Outline each blood parasite and name the species.
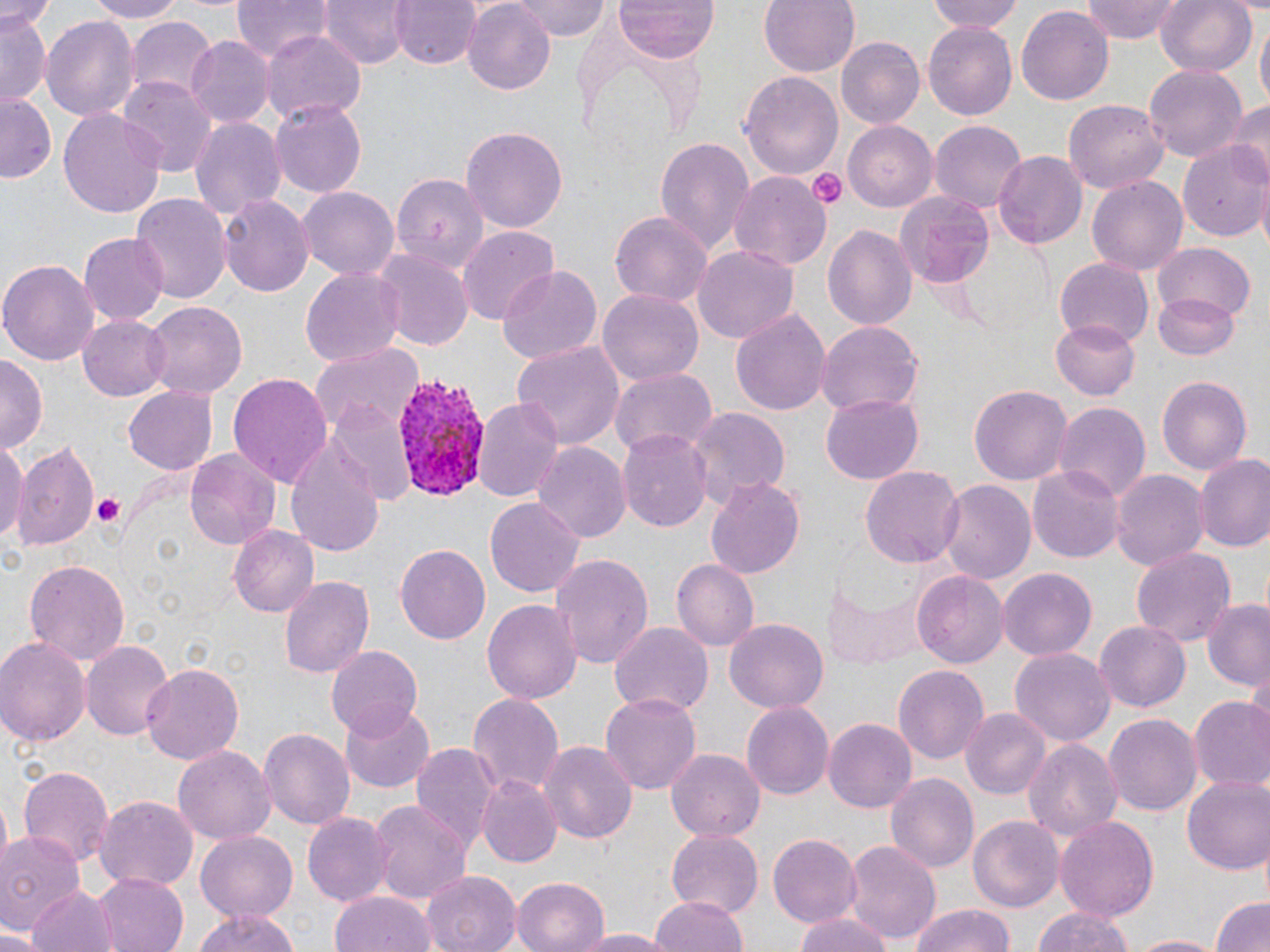

Approximate bounding boxes as named x1/y1/x2/y2 corners in pixels.
Plasmodium vivax-infected red blood cells: (x1=393, y1=371, x2=491, y2=504).
No Plasmodium falciparum, Plasmodium ovale, Plasmodium malariae, Babesia divergens, or Trypanosoma brucei observed.

slide-level diagnosis = Plasmodium vivax
magnification = 1000x
stain = May-Grünwald-Giemsa
platelet locations = approximate bounding boxes as named x1/y1/x2/y2 corners in pixels: (x1=808, y1=169, x2=847, y2=208), (x1=89, y1=493, x2=128, y2=530)
modality = optical microscopy
field of view = single
image size = 1270×952 pixels
preparation = thin blood smear
uninfected red blood cell locations = approximate bounding boxes as named x1/y1/x2/y2 corners in pixels: (x1=0, y1=0, x2=56, y2=28), (x1=81, y1=0, x2=192, y2=22), (x1=232, y1=0, x2=327, y2=62), (x1=318, y1=0, x2=411, y2=68), (x1=393, y1=0, x2=479, y2=69), (x1=511, y1=0, x2=609, y2=41), (x1=613, y1=0, x2=718, y2=62), (x1=757, y1=0, x2=859, y2=77), (x1=928, y1=0, x2=1023, y2=35), (x1=1080, y1=0, x2=1184, y2=42), (x1=1153, y1=0, x2=1256, y2=77), (x1=1015, y1=3, x2=1114, y2=104), (x1=462, y1=4, x2=557, y2=94), (x1=0, y1=8, x2=48, y2=108), (x1=41, y1=12, x2=139, y2=121), (x1=125, y1=17, x2=216, y2=102), (x1=1255, y1=19, x2=1269, y2=112), (x1=924, y1=20, x2=1019, y2=120), (x1=262, y1=30, x2=364, y2=124), (x1=186, y1=37, x2=274, y2=127), (x1=834, y1=37, x2=924, y2=130), (x1=1143, y1=65, x2=1248, y2=163), (x1=739, y1=68, x2=844, y2=180), (x1=118, y1=78, x2=216, y2=175), (x1=0, y1=95, x2=56, y2=183), (x1=1222, y1=95, x2=1270, y2=183), (x1=1062, y1=98, x2=1168, y2=195), (x1=271, y1=101, x2=370, y2=197), (x1=59, y1=108, x2=166, y2=218), (x1=190, y1=116, x2=284, y2=222), (x1=931, y1=120, x2=1026, y2=217), (x1=844, y1=121, x2=937, y2=208), (x1=461, y1=127, x2=567, y2=232), (x1=654, y1=136, x2=754, y2=256), (x1=1182, y1=139, x2=1270, y2=242), (x1=994, y1=151, x2=1085, y2=251), (x1=392, y1=171, x2=485, y2=262), (x1=728, y1=171, x2=833, y2=270), (x1=1087, y1=174, x2=1188, y2=273), (x1=296, y1=187, x2=402, y2=282), (x1=897, y1=192, x2=993, y2=288), (x1=131, y1=194, x2=228, y2=307), (x1=217, y1=194, x2=312, y2=298), (x1=610, y1=209, x2=713, y2=311), (x1=822, y1=225, x2=916, y2=332), (x1=458, y1=226, x2=561, y2=324), (x1=79, y1=233, x2=170, y2=324), (x1=1153, y1=243, x2=1256, y2=323), (x1=692, y1=245, x2=798, y2=344), (x1=372, y1=248, x2=472, y2=352), (x1=1, y1=258, x2=99, y2=366), (x1=1055, y1=258, x2=1153, y2=348), (x1=495, y1=265, x2=602, y2=367), (x1=300, y1=268, x2=405, y2=366), (x1=599, y1=287, x2=705, y2=388), (x1=1153, y1=291, x2=1240, y2=358), (x1=142, y1=300, x2=248, y2=398), (x1=731, y1=307, x2=830, y2=415), (x1=78, y1=315, x2=172, y2=400), (x1=1052, y1=318, x2=1141, y2=401), (x1=816, y1=320, x2=924, y2=417), (x1=512, y1=337, x2=625, y2=450), (x1=314, y1=344, x2=423, y2=436), (x1=0, y1=354, x2=44, y2=451), (x1=610, y1=365, x2=717, y2=458), (x1=227, y1=369, x2=334, y2=485), (x1=1154, y1=373, x2=1256, y2=478), (x1=969, y1=383, x2=1072, y2=484), (x1=122, y1=386, x2=217, y2=475), (x1=475, y1=395, x2=565, y2=504), (x1=821, y1=395, x2=924, y2=483), (x1=1055, y1=403, x2=1150, y2=507), (x1=328, y1=404, x2=417, y2=506), (x1=689, y1=409, x2=787, y2=504), (x1=616, y1=430, x2=713, y2=529), (x1=286, y1=434, x2=387, y2=559), (x1=0, y1=436, x2=25, y2=542), (x1=8, y1=439, x2=101, y2=553), (x1=531, y1=440, x2=629, y2=541), (x1=184, y1=450, x2=280, y2=549), (x1=1196, y1=455, x2=1270, y2=554), (x1=1028, y1=461, x2=1124, y2=564), (x1=861, y1=465, x2=963, y2=570), (x1=1113, y1=468, x2=1208, y2=571), (x1=705, y1=478, x2=807, y2=579), (x1=939, y1=480, x2=1034, y2=586), (x1=485, y1=497, x2=583, y2=595), (x1=230, y1=525, x2=321, y2=616), (x1=396, y1=543, x2=493, y2=645), (x1=1131, y1=545, x2=1234, y2=651), (x1=552, y1=553, x2=655, y2=670), (x1=25, y1=558, x2=130, y2=666), (x1=672, y1=560, x2=759, y2=648), (x1=998, y1=568, x2=1096, y2=659), (x1=913, y1=569, x2=1007, y2=669), (x1=280, y1=576, x2=373, y2=681), (x1=826, y1=579, x2=923, y2=667), (x1=482, y1=596, x2=580, y2=701), (x1=1201, y1=600, x2=1270, y2=692), (x1=1093, y1=618, x2=1191, y2=713), (x1=725, y1=619, x2=829, y2=714), (x1=609, y1=620, x2=712, y2=717), (x1=0, y1=635, x2=88, y2=752), (x1=81, y1=640, x2=179, y2=742), (x1=326, y1=646, x2=422, y2=739), (x1=1011, y1=649, x2=1115, y2=748), (x1=140, y1=662, x2=245, y2=765), (x1=894, y1=665, x2=989, y2=764), (x1=468, y1=690, x2=563, y2=795), (x1=601, y1=692, x2=699, y2=792), (x1=1189, y1=697, x2=1270, y2=791), (x1=340, y1=698, x2=434, y2=792), (x1=741, y1=700, x2=833, y2=799), (x1=962, y1=708, x2=1051, y2=799), (x1=1103, y1=711, x2=1201, y2=816), (x1=823, y1=718, x2=915, y2=812), (x1=258, y1=728, x2=356, y2=830), (x1=1023, y1=738, x2=1123, y2=840), (x1=536, y1=740, x2=638, y2=845), (x1=409, y1=741, x2=499, y2=852), (x1=172, y1=744, x2=278, y2=845), (x1=664, y1=745, x2=768, y2=842), (x1=18, y1=763, x2=114, y2=870), (x1=885, y1=773, x2=979, y2=871), (x1=1183, y1=774, x2=1270, y2=876), (x1=475, y1=775, x2=561, y2=869), (x1=95, y1=796, x2=197, y2=891), (x1=371, y1=801, x2=470, y2=906), (x1=302, y1=810, x2=392, y2=906), (x1=969, y1=815, x2=1065, y2=913), (x1=1054, y1=815, x2=1161, y2=924), (x1=194, y1=830, x2=298, y2=922), (x1=666, y1=830, x2=763, y2=915), (x1=0, y1=831, x2=84, y2=933), (x1=769, y1=834, x2=860, y2=922), (x1=845, y1=841, x2=941, y2=944), (x1=420, y1=869, x2=520, y2=952), (x1=94, y1=872, x2=190, y2=952), (x1=512, y1=875, x2=612, y2=952), (x1=27, y1=884, x2=114, y2=952), (x1=331, y1=893, x2=435, y2=952), (x1=1210, y1=894, x2=1270, y2=952), (x1=651, y1=895, x2=749, y2=952), (x1=908, y1=903, x2=1017, y2=952), (x1=1029, y1=904, x2=1142, y2=952), (x1=187, y1=909, x2=303, y2=952), (x1=790, y1=911, x2=900, y2=952), (x1=0, y1=928, x2=43, y2=952), (x1=566, y1=928, x2=680, y2=950), (x1=1127, y1=933, x2=1224, y2=952)